Assess the morphology of the erythrocytes.
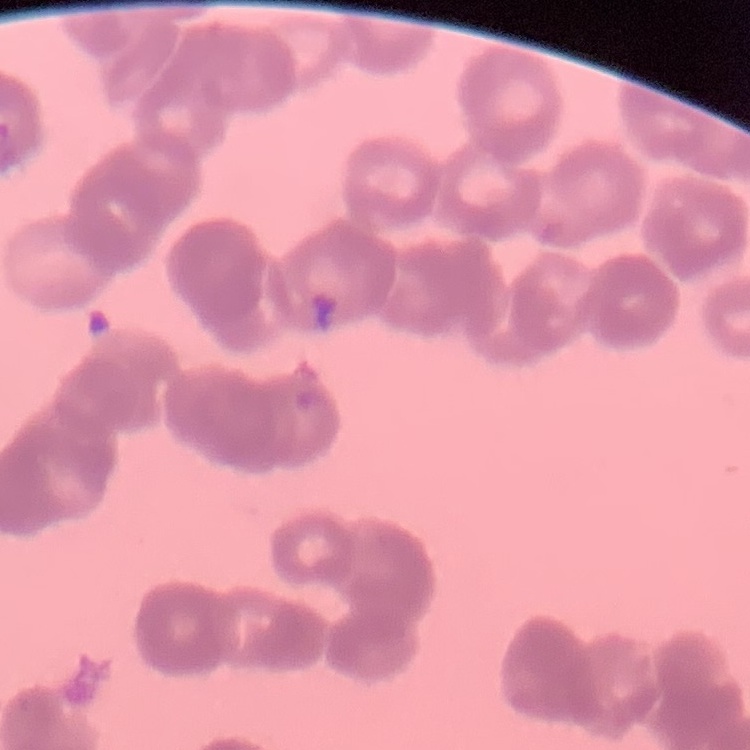
They show rouleaux formation.

{
  "stain": "Field's or Giemsa",
  "preparation": "thin peripheral smear",
  "image_type": "square crop of a larger photomicrograph"
}